Assess the morphology of the erythrocytes.
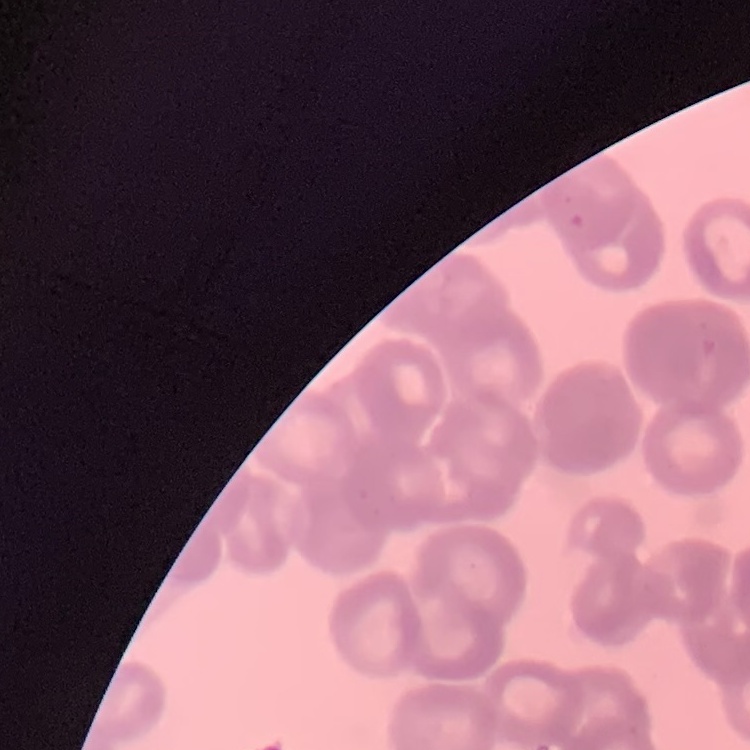

Rouleaux formation.

stain = Field's or Giemsa
preparation = thin blood smear
image type = square crop of a larger photomicrograph